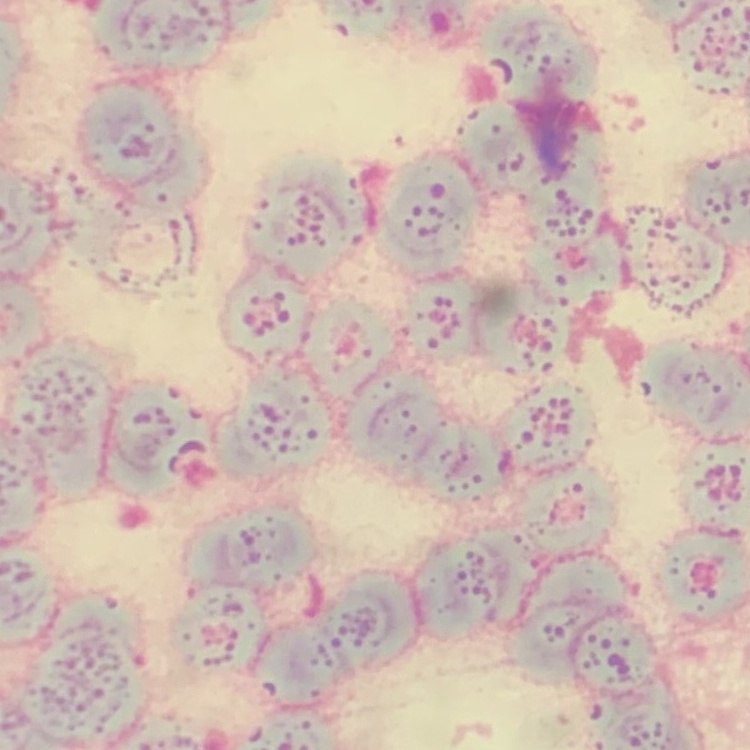 The erythrocytes show rouleaux formation. Square crop of a larger photomicrograph. Thin blood smear. Field's or Giemsa stain.